Identify the blood parasite species.
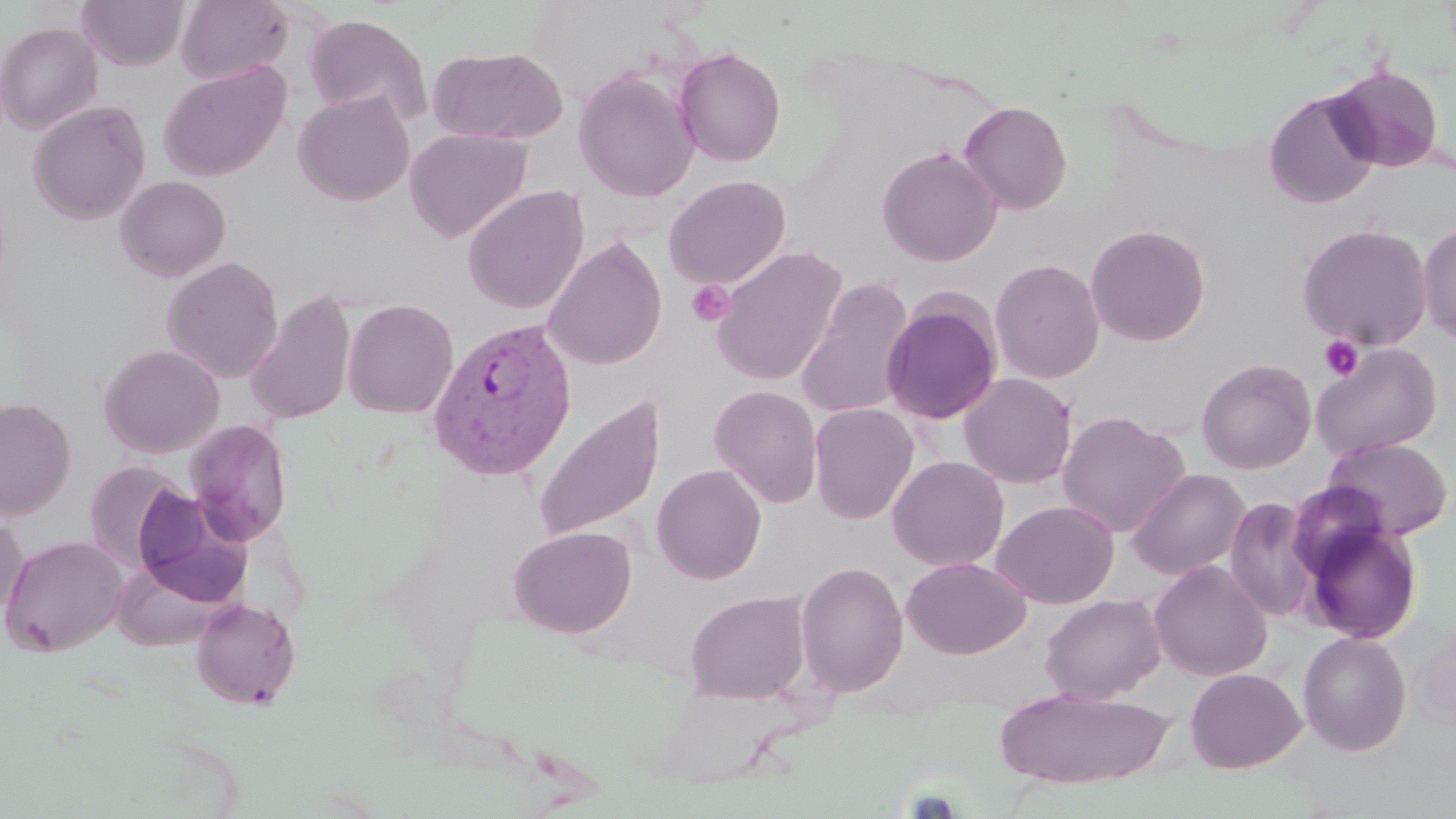
Plasmodium vivax.

Summary:
  - Coordinate format: approximate bounding boxes as named x1/y1/x2/y2 corners in pixels
  - Uninfected red blood cell locations: (x1=175, y1=0, x2=293, y2=85), (x1=77, y1=1, x2=188, y2=70), (x1=304, y1=12, x2=432, y2=126), (x1=0, y1=21, x2=103, y2=135), (x1=428, y1=46, x2=567, y2=145), (x1=674, y1=46, x2=786, y2=167), (x1=159, y1=60, x2=291, y2=181), (x1=1329, y1=64, x2=1445, y2=172), (x1=573, y1=68, x2=699, y2=202), (x1=1263, y1=90, x2=1381, y2=210), (x1=293, y1=91, x2=414, y2=206), (x1=28, y1=100, x2=150, y2=225), (x1=958, y1=100, x2=1072, y2=215), (x1=405, y1=127, x2=532, y2=243), (x1=877, y1=145, x2=1002, y2=267), (x1=115, y1=175, x2=231, y2=281), (x1=664, y1=175, x2=791, y2=289), (x1=462, y1=186, x2=588, y2=315), (x1=1417, y1=221, x2=1456, y2=344), (x1=1296, y1=222, x2=1433, y2=350), (x1=1085, y1=223, x2=1211, y2=347), (x1=542, y1=237, x2=667, y2=371), (x1=710, y1=246, x2=848, y2=386), (x1=161, y1=256, x2=284, y2=383), (x1=990, y1=258, x2=1105, y2=383), (x1=795, y1=277, x2=916, y2=420), (x1=244, y1=289, x2=357, y2=426), (x1=880, y1=297, x2=1002, y2=425), (x1=341, y1=298, x2=459, y2=418), (x1=1311, y1=342, x2=1443, y2=460), (x1=98, y1=344, x2=224, y2=458), (x1=1196, y1=358, x2=1317, y2=474), (x1=958, y1=372, x2=1078, y2=489), (x1=709, y1=385, x2=823, y2=507), (x1=533, y1=394, x2=666, y2=544), (x1=1, y1=398, x2=76, y2=520), (x1=809, y1=403, x2=919, y2=525), (x1=1057, y1=411, x2=1190, y2=538), (x1=184, y1=419, x2=293, y2=546), (x1=1322, y1=436, x2=1453, y2=541), (x1=887, y1=455, x2=1009, y2=571), (x1=83, y1=460, x2=188, y2=572), (x1=651, y1=464, x2=766, y2=584), (x1=1126, y1=468, x2=1250, y2=580), (x1=132, y1=487, x2=252, y2=607), (x1=1224, y1=496, x2=1320, y2=622), (x1=992, y1=500, x2=1119, y2=609), (x1=0, y1=513, x2=27, y2=625), (x1=1301, y1=521, x2=1423, y2=645), (x1=509, y1=525, x2=637, y2=638), (x1=1, y1=534, x2=129, y2=656), (x1=901, y1=556, x2=1031, y2=659), (x1=112, y1=559, x2=234, y2=651), (x1=795, y1=560, x2=909, y2=697), (x1=1149, y1=560, x2=1272, y2=681), (x1=684, y1=590, x2=810, y2=705), (x1=1040, y1=593, x2=1166, y2=704), (x1=190, y1=598, x2=301, y2=709), (x1=1412, y1=620, x2=1456, y2=735), (x1=1298, y1=631, x2=1412, y2=755), (x1=1185, y1=667, x2=1306, y2=774), (x1=994, y1=686, x2=1174, y2=790)
  - Plasmodium vivax-infected red blood cell locations: (x1=425, y1=316, x2=578, y2=481)
  - Platelet locations: (x1=686, y1=279, x2=736, y2=327), (x1=1319, y1=335, x2=1364, y2=382)
  - Stain: May-Grünwald-Giemsa
  - Preparation: thin blood smear
  - Magnification: 1000x
  - Modality: optical microscopy
  - Field of view: single
  - Image size: 1456×819 pixels